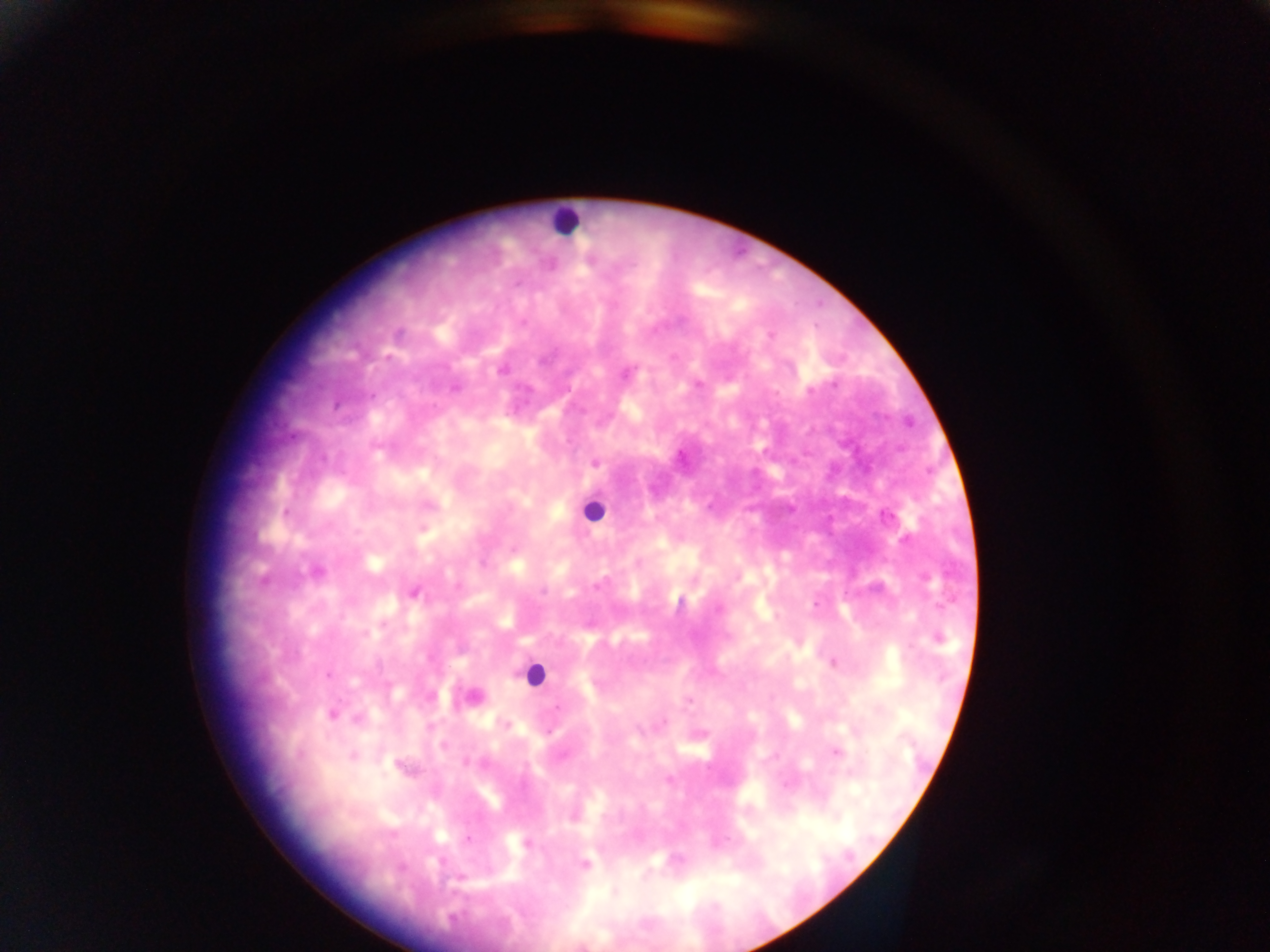
country = Ghana
leukocyte locations = approximate centers as [x, y] in pixels: [566, 220], [592, 510], [534, 673]
capture = mobile-phone photograph through a microscope
preparation = thick blood film
image size = 1270×952 pixels
field of view = single
malaria parasite locations = approximate centers as [x, y] in pixels: [770, 335], [626, 372], [697, 384], [595, 461], [423, 528], [315, 572], [414, 592], [716, 609], [937, 638], [832, 662], [471, 696], [687, 699], [330, 714], [359, 718], [505, 724], [836, 752], [352, 756], [401, 767], [573, 815], [526, 844], [584, 864], [614, 892]